Assess the morphology of the erythrocytes.
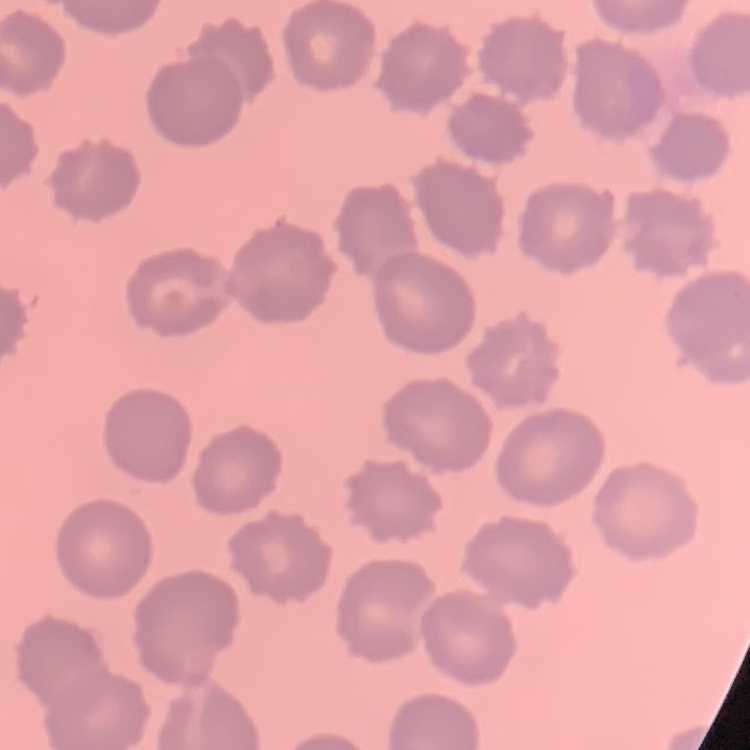

They show no rouleaux formation.

Summary:
  - Preparation: thin blood film
  - Image type: square crop of a larger photomicrograph
  - Stain: Field's or Giemsa